State the blood parasite species.
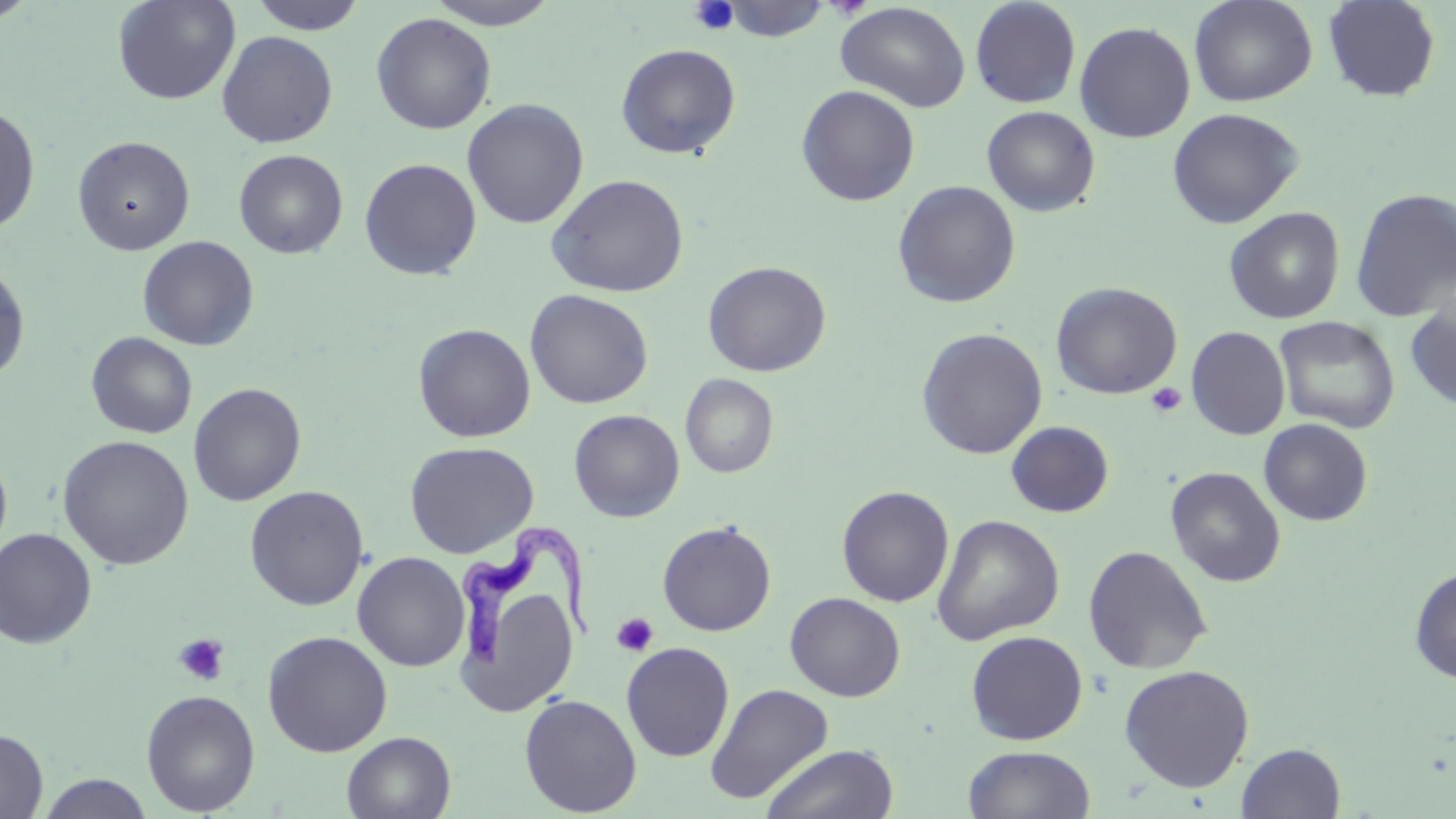
Trypanosoma brucei.

preparation = thin blood smear
stain = May-Grünwald-Giemsa
magnification = 1000x
image size = 1456×819 pixels
modality = light microscopy
uninfected red blood cell locations = approximate bounding boxes as [x1, y1, x2, y2] in pixels: [0, 0, 39, 25], [112, 0, 241, 105], [248, 0, 367, 35], [423, 0, 562, 29], [970, 0, 1081, 108], [1189, 0, 1317, 107], [1322, 0, 1441, 102], [720, 1, 832, 42], [835, 2, 971, 112], [371, 13, 496, 134], [1074, 21, 1196, 143], [216, 30, 338, 148], [616, 43, 741, 159], [796, 85, 920, 206], [462, 98, 589, 229], [0, 103, 40, 235], [982, 106, 1100, 216], [1166, 107, 1304, 229], [72, 135, 195, 256], [233, 149, 348, 259], [359, 158, 482, 280], [546, 174, 689, 298], [893, 180, 1021, 308], [1350, 188, 1456, 323], [1224, 207, 1345, 324], [137, 235, 259, 351], [703, 260, 831, 377], [0, 263, 31, 385], [1050, 281, 1182, 399], [1405, 287, 1456, 412], [525, 289, 653, 409], [1274, 316, 1400, 434], [413, 323, 536, 442], [1186, 326, 1290, 440], [916, 327, 1048, 459], [86, 332, 197, 439], [681, 374, 778, 478], [188, 383, 307, 506], [568, 409, 684, 522], [1259, 418, 1372, 526], [1006, 420, 1114, 518], [57, 435, 195, 570], [404, 441, 538, 558], [0, 448, 13, 568], [1165, 466, 1286, 587], [244, 485, 369, 611], [837, 485, 954, 607], [931, 514, 1065, 645], [657, 520, 776, 636], [0, 528, 98, 648], [1083, 545, 1214, 675], [352, 552, 470, 672], [1409, 565, 1456, 683], [785, 592, 905, 702], [453, 593, 579, 725], [262, 630, 393, 757], [965, 630, 1088, 745], [621, 642, 734, 762], [1119, 663, 1255, 792], [705, 683, 834, 805], [141, 689, 261, 816], [519, 694, 642, 816], [0, 729, 48, 818], [342, 731, 456, 819], [760, 743, 899, 819], [1237, 743, 1346, 819], [962, 745, 1096, 819], [38, 773, 155, 818]
Trypanosoma brucei locations = approximate bounding boxes as [x1, y1, x2, y2] in pixels: [452, 523, 584, 665]
field of view = single
platelet locations = approximate bounding boxes as [x1, y1, x2, y2] in pixels: [689, 0, 739, 37], [1146, 382, 1187, 419], [611, 612, 658, 658], [172, 633, 230, 686]